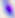
Summary:
  - Modality: photomicrograph
  - Magnification: 400x
  - Identification: Toxoplasma gondii